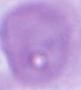 Captured at 1000x magnification. An erythrocyte is seen. Micrograph.